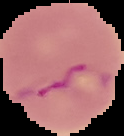
Image is 124×136 pixels. Malaria status: parasitized. From a thin blood smear. The area outside the segmented cell region is set to black.